Report the malaria status of this cell.
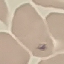
It is parasitized.

Thin blood film. Giemsa-stained preparation. Acquired by smartphone through the microscope eyepiece. Cell patch, automatically extracted from a larger field of view and resized to 64 × 64 pixels.